Name the blood parasite species.
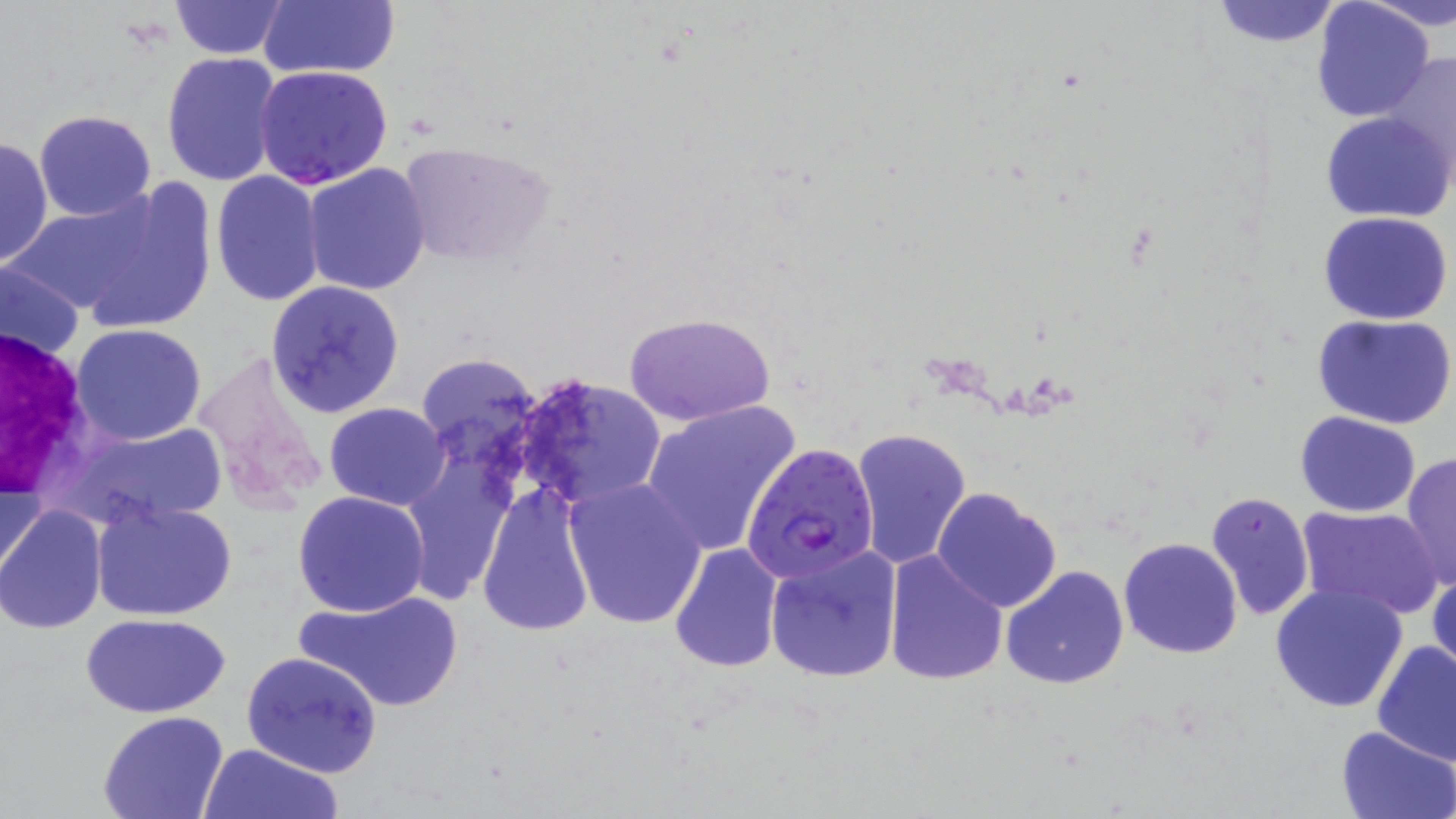

Plasmodium falciparum.

Summary:
  - Coordinate format: approximate bounding boxes as (x1, y1, x2, y2) in pixels
  - Plasmodium falciparum-infected red blood cell locations: (742, 442, 880, 582)
  - White blood cell locations: (3, 327, 99, 502)
  - Uninfected red blood cell locations: (168, 0, 288, 59), (1207, 0, 1346, 48), (1364, 0, 1456, 34), (258, 1, 400, 80), (1310, 1, 1435, 120), (1375, 51, 1456, 184), (161, 52, 282, 187), (254, 65, 394, 190), (33, 110, 158, 221), (1321, 111, 1454, 224), (0, 137, 52, 267), (396, 137, 557, 267), (302, 164, 432, 295), (210, 170, 326, 305), (72, 176, 215, 336), (6, 187, 179, 321), (1318, 210, 1453, 325), (1, 256, 84, 368), (267, 281, 405, 417), (624, 311, 777, 424), (1312, 313, 1455, 430), (71, 324, 207, 445), (414, 353, 543, 474), (515, 372, 668, 510), (640, 400, 800, 558), (324, 402, 450, 510), (1294, 411, 1421, 516), (59, 421, 228, 531), (850, 427, 972, 569), (1400, 452, 1456, 593), (0, 455, 46, 583), (401, 459, 517, 604), (563, 477, 705, 630), (478, 485, 596, 637), (931, 486, 1062, 612), (293, 490, 430, 617), (1206, 492, 1312, 620), (91, 501, 237, 622), (0, 504, 108, 633), (1296, 506, 1442, 620), (1118, 536, 1244, 659), (667, 542, 785, 673), (764, 545, 904, 683), (883, 550, 1008, 685), (1001, 565, 1130, 689), (1429, 566, 1456, 681), (1269, 584, 1410, 715), (294, 589, 465, 712), (80, 612, 231, 718), (1373, 641, 1456, 768), (241, 651, 383, 777), (99, 711, 228, 819), (1334, 726, 1456, 819), (200, 743, 342, 819)
  - Image size: 1456×819 pixels
  - Field of view: single
  - Preparation: thin blood smear
  - Magnification: 1000x
  - Modality: light microscopy
  - Stain: May-Grünwald-Giemsa